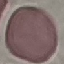

Summary:
  - Malaria status: uninfected
  - Image type: automatically extracted cell patch, resized to 64 × 64 pixels
  - Capture: smartphone through the microscope eyepiece
  - Preparation: thin smear
  - Stain: Giemsa